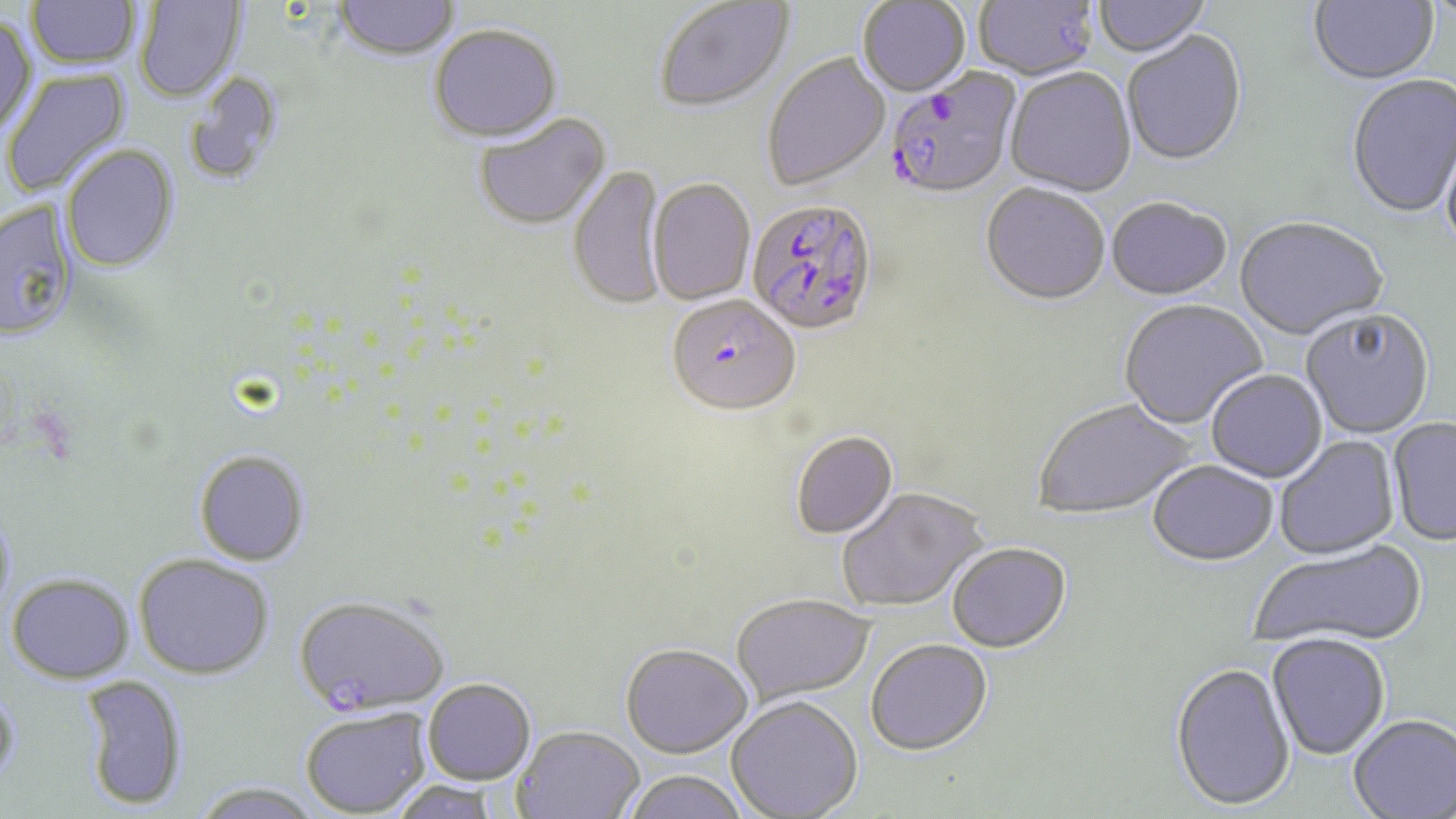 Approximate bounding boxes as [x1, y1, x2, y2] in pixels. Plasmodium falciparum-infected red blood cell locations: [884, 71, 1021, 203], [747, 201, 879, 339], [667, 299, 800, 420]. Uninfected red blood cell locations: [25, 0, 140, 73], [858, 0, 970, 99], [974, 0, 1098, 82], [1093, 0, 1212, 60], [1309, 0, 1440, 88], [135, 1, 246, 104], [332, 1, 461, 63], [656, 1, 795, 115], [0, 17, 38, 137], [429, 26, 563, 147], [1122, 32, 1247, 169], [762, 54, 891, 192], [2, 67, 132, 198], [1004, 69, 1137, 199], [183, 70, 286, 187], [1346, 76, 1456, 220], [474, 114, 612, 233], [1440, 129, 1456, 263], [60, 145, 180, 275], [568, 164, 668, 314], [647, 179, 755, 307], [980, 185, 1109, 308], [1105, 200, 1232, 303], [0, 201, 78, 343], [1234, 219, 1388, 343], [1119, 301, 1268, 431], [1301, 311, 1435, 440], [1206, 371, 1327, 484], [1034, 400, 1196, 522], [1386, 418, 1456, 548], [791, 433, 899, 540], [1274, 435, 1401, 562], [194, 452, 310, 568], [1147, 463, 1278, 569], [838, 489, 990, 613], [0, 506, 17, 627], [1249, 542, 1427, 652], [947, 545, 1071, 656], [134, 555, 274, 681], [6, 574, 134, 685], [292, 597, 449, 719], [732, 597, 875, 707], [1267, 636, 1390, 761], [866, 641, 993, 759], [620, 647, 752, 762], [1169, 665, 1296, 814], [78, 676, 187, 811], [422, 681, 536, 787], [0, 682, 24, 792], [726, 698, 863, 819], [300, 710, 430, 818], [1348, 715, 1456, 818], [512, 728, 645, 818], [622, 772, 750, 819], [189, 781, 325, 819], [388, 782, 503, 819]. Slide-level diagnosis: Plasmodium falciparum. Single field of view. May-Grünwald-Giemsa-stained preparation. Light microscopy. 1000x magnification. Image is 1456×819 pixels. Thin blood film.